State which parasite is depicted.
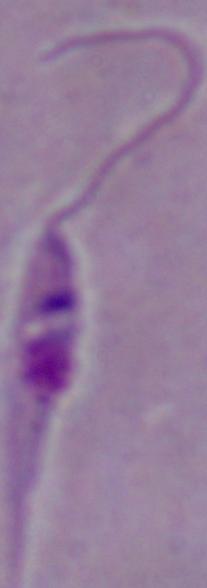
This is Leishmania.

Captured at 1000x magnification. Micrograph.